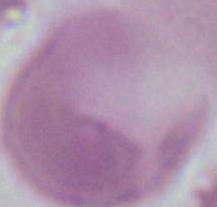
Summary:
  - Magnification: 1000x
  - Modality: photomicrograph
  - Identification: erythrocyte